Name the parasite shown.
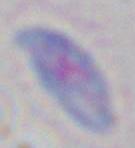
This is Toxoplasma gondii.

Photomicrograph. 1000x magnification.